Assess this cell for malaria.
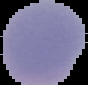
It is uninfected.

Segmented cell region on a black background. From a thin blood film. Image is 88×85 pixels.